Describe the morphology of the erythrocytes.
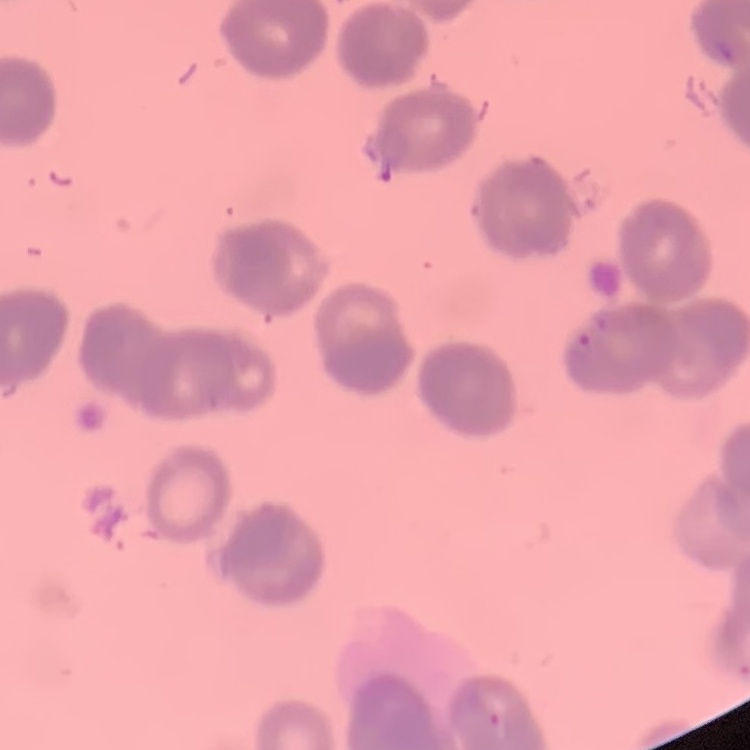

They show rouleaux formation.

Square crop of a larger photomicrograph. Thin peripheral smear. Field's or Giemsa stain.